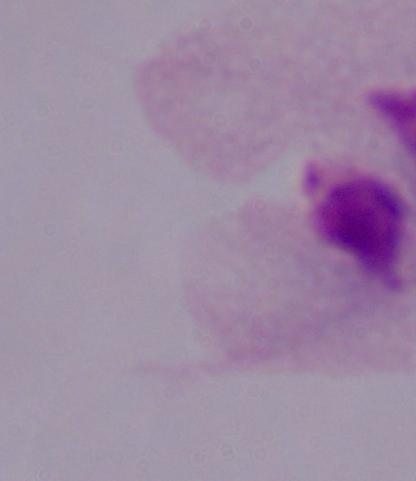

magnification = 1000x
identification = trichomonad
modality = photomicrograph